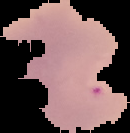
image size = 130×133 pixels
malaria status = parasitized
image type = cell region segmented out of the field of view; surrounding area masked to black
preparation = thin blood smear